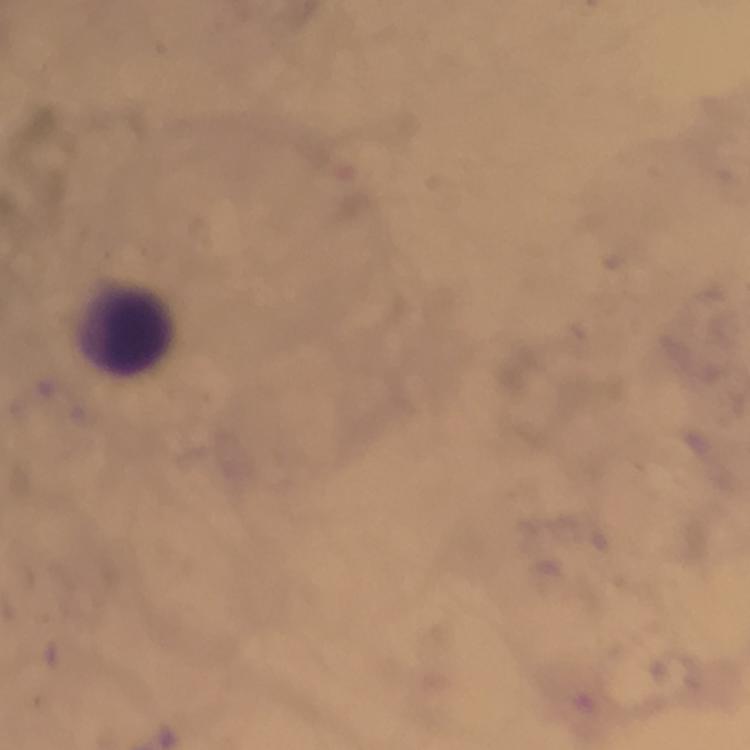
Approximate centers as [x, y] in pixels. Leukocyte locations: [126, 331]. Thick blood film. At 100x magnification. Malaria parasites: none detected. Photographed through the microscope with a smartphone camera. From a diagnostic examination for malaria. Immersion oil applied. Image is 750×750 pixels. A crop from one field of view. Giemsa stain.